Identify the parasite.
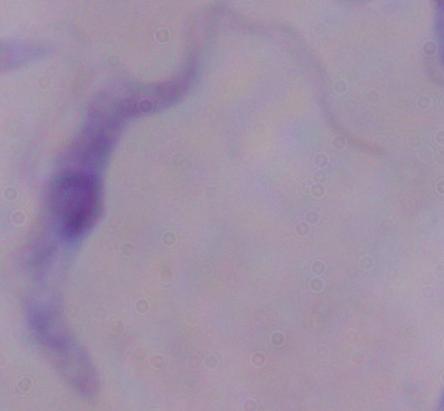
A trypanosome.

Micrograph. 1000x magnification.